Identify the cell.
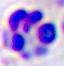
A leukocyte.

Micrograph. Captured at 400x magnification.